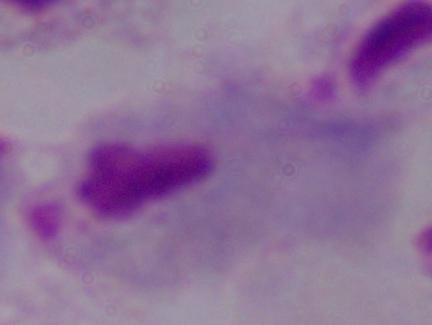

{
  "identification": "trichomonad",
  "magnification": "1000x",
  "modality": "photomicrograph"
}